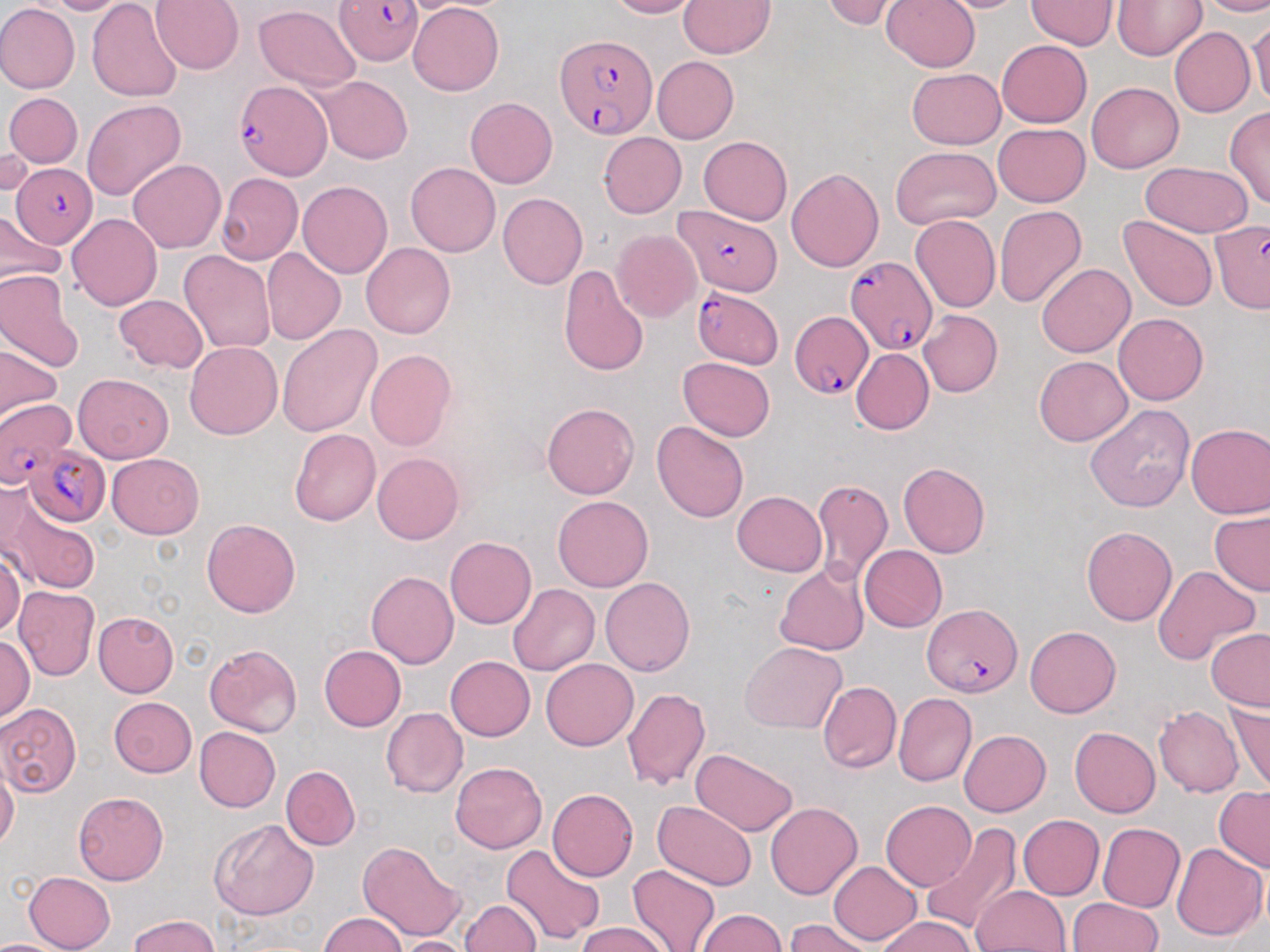
{
  "plasmodium_falciparum_infected_red_blood_cell_locations_subset": "approximate bounding boxes as (x1, y1, x2, y2) in pixels: (334, 0, 422, 66), (556, 35, 656, 139), (233, 83, 330, 178), (12, 163, 97, 247), (673, 207, 781, 294), (1211, 218, 1270, 310), (847, 255, 938, 358), (692, 287, 784, 369), (791, 310, 874, 400), (0, 399, 75, 486), (26, 444, 111, 526), (923, 604, 1021, 697)",
  "slide_level_diagnosis": "Plasmodium falciparum",
  "field_of_view": "single",
  "modality": "optical microscopy",
  "image_size": "1270×952 pixels",
  "magnification": "1000x",
  "uninfected_red_blood_cell_locations_subset": "approximate bounding boxes as (x1, y1, x2, y2) in pixels: (41, 0, 134, 15), (152, 0, 244, 74), (606, 0, 700, 19), (679, 0, 774, 57), (820, 0, 908, 29), (881, 0, 980, 73), (932, 0, 1032, 13), (1026, 0, 1117, 50), (1114, 0, 1207, 60), (1200, 0, 1270, 17), (88, 1, 183, 104), (409, 2, 504, 96), (0, 3, 80, 94), (254, 5, 360, 91), (1247, 13, 1270, 110), (1169, 27, 1254, 118), (996, 40, 1092, 128), (652, 56, 738, 144), (908, 68, 1005, 149), (315, 76, 412, 164), (1085, 82, 1184, 173), (4, 92, 82, 169), (466, 96, 557, 187), (82, 98, 186, 199), (1224, 107, 1270, 210), (993, 123, 1090, 207), (599, 132, 686, 217), (699, 136, 792, 225), (1, 138, 35, 201), (891, 147, 1001, 228), (128, 159, 225, 253), (1138, 161, 1254, 238), (406, 163, 501, 257), (786, 168, 884, 271), (215, 174, 302, 265), (298, 181, 392, 278), (497, 193, 588, 289), (995, 206, 1087, 309), (67, 214, 162, 310), (910, 214, 1001, 313), (1119, 215, 1218, 312), (612, 229, 700, 323), (361, 242, 456, 339), (261, 248, 347, 346), (179, 250, 275, 356), (1037, 263, 1135, 357), (556, 266, 649, 377), (0, 271, 83, 372), (114, 294, 208, 374), (918, 310, 1002, 398), (1114, 313, 1208, 406), (276, 323, 382, 437), (185, 341, 282, 439), (0, 343, 63, 423), (365, 349, 456, 451), (851, 349, 933, 434), (1035, 356, 1132, 446), (678, 358, 775, 442), (72, 372, 173, 462), (542, 402, 639, 499), (1085, 404, 1195, 513), (653, 422, 749, 523), (1186, 424, 1270, 518), (290, 429, 380, 525), (372, 452, 464, 544), (106, 453, 204, 539), (898, 462, 990, 559), (812, 478, 892, 584), (2, 488, 100, 596), (733, 491, 827, 576), (552, 494, 653, 592), (1209, 509, 1270, 597), (201, 519, 300, 617), (1081, 525, 1178, 625), (444, 536, 537, 629), (859, 545, 947, 631), (0, 552, 25, 638), (774, 562, 870, 656), (1151, 564, 1260, 667), (366, 571, 459, 668), (601, 577, 695, 676), (508, 584, 600, 675), (13, 586, 99, 681), (93, 611, 179, 697), (1025, 626, 1121, 717), (1205, 628, 1270, 711), (0, 636, 34, 722), (740, 641, 846, 733), (203, 644, 302, 738), (319, 645, 405, 731), (446, 656, 535, 740), (541, 658, 638, 751), (818, 681, 901, 772), (622, 687, 711, 791), (892, 693, 976, 787), (109, 697, 197, 777), (1227, 699, 1270, 791), (1, 703, 82, 796), (1154, 705, 1244, 797), (380, 706, 468, 798), (194, 726, 281, 812), (1069, 726, 1160, 818), (959, 730, 1051, 817), (690, 748, 798, 836), (449, 761, 547, 854), (0, 763, 19, 851), (282, 766, 360, 850), (1214, 786, 1270, 873), (547, 789, 637, 881), (73, 791, 170, 885), (654, 800, 757, 892), (881, 801, 976, 890), (766, 803, 862, 900), (1018, 815, 1104, 898), (209, 818, 319, 920), (1097, 823, 1185, 912), (921, 824, 1022, 933), (358, 842, 467, 942), (1169, 842, 1268, 942), (500, 844, 605, 946), (829, 861, 922, 946), (628, 864, 720, 952), (23, 871, 116, 952), (972, 885, 1070, 951), (1068, 898, 1162, 951), (460, 901, 541, 952), (695, 909, 786, 951), (318, 913, 406, 951), (128, 914, 220, 952), (877, 917, 976, 952), (785, 918, 875, 952), (576, 923, 670, 952), (392, 936, 476, 952), (0, 939, 62, 951)",
  "preparation": "thin blood film",
  "stain": "May-Grünwald-Giemsa"
}